Describe the morphology of the red blood cells.
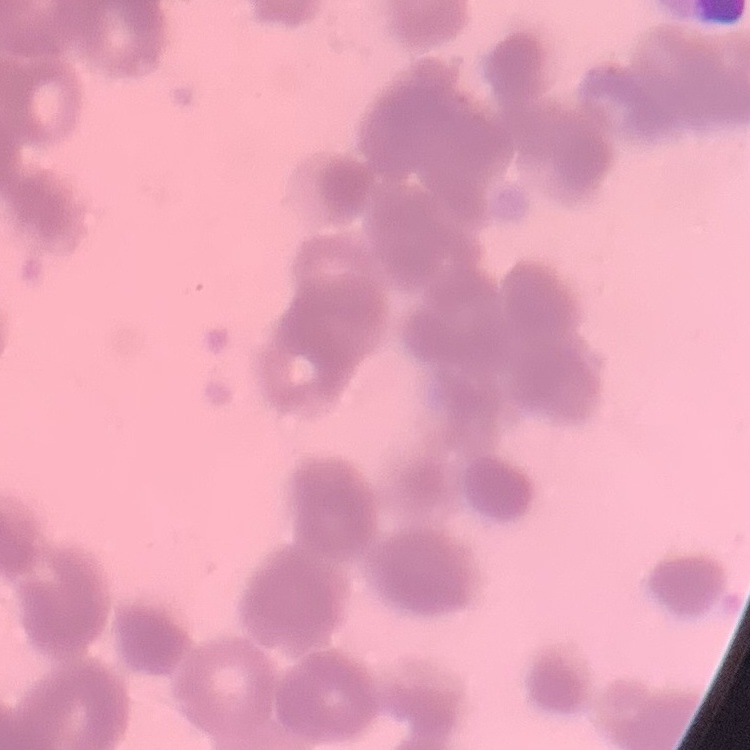

Rouleaux formation.

Stained with either Field's or Giemsa. One tile cut from a larger photomicrograph. Thin blood smear.